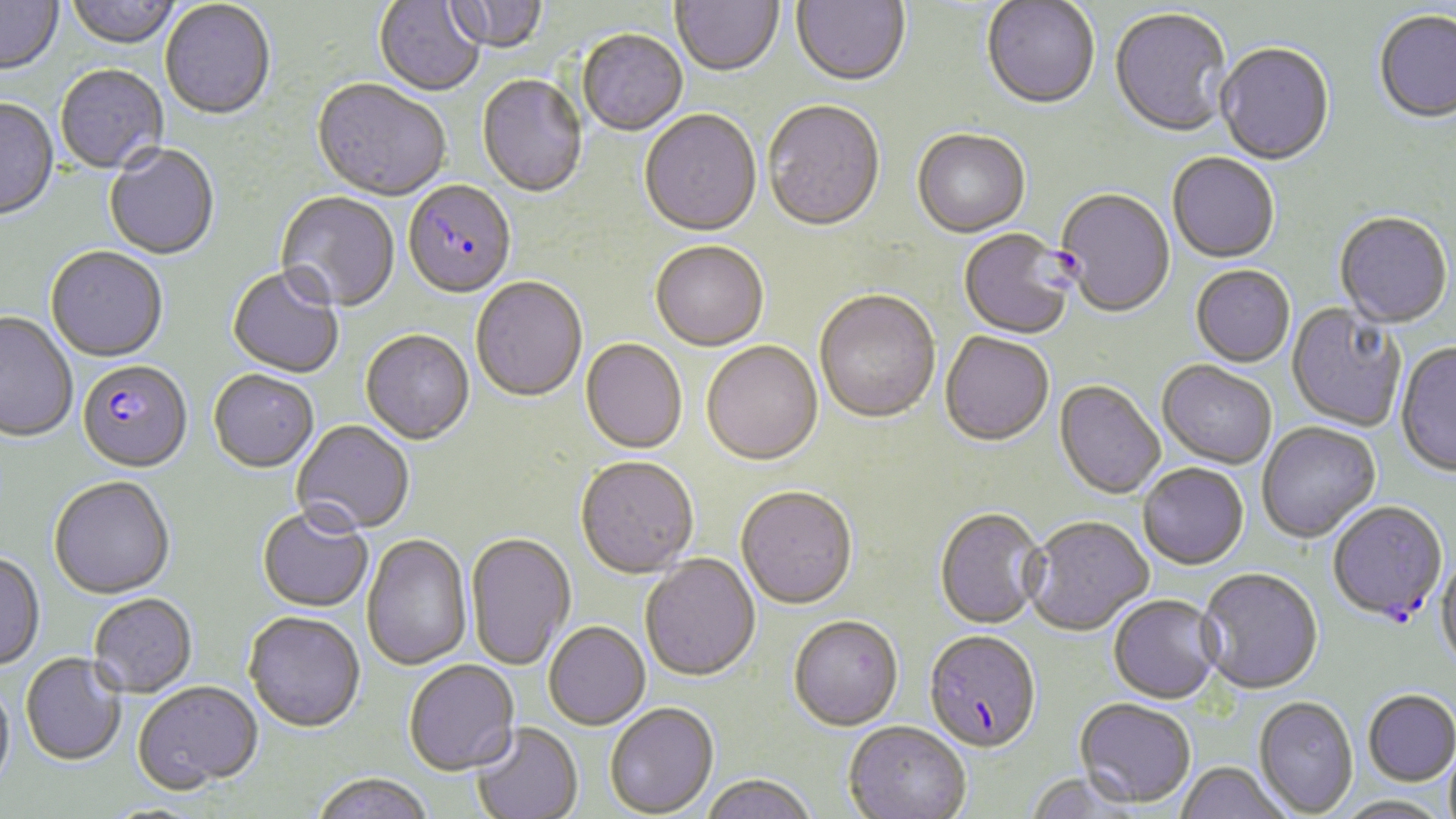
Approximate bounding boxes as (x1, y1, x2, y2) in pixels. Plasmodium falciparum-infected red blood cell locations: (403, 183, 516, 300), (958, 230, 1075, 342), (77, 362, 192, 475), (1328, 503, 1448, 626), (923, 634, 1042, 757). Uninfected red blood cell locations: (0, 0, 63, 77), (65, 0, 182, 51), (374, 0, 485, 98), (442, 0, 548, 55), (671, 0, 784, 79), (791, 0, 910, 89), (981, 1, 1100, 112), (160, 2, 275, 123), (1109, 9, 1232, 140), (1374, 12, 1456, 126), (578, 31, 688, 137), (1216, 45, 1335, 167), (56, 66, 168, 175), (477, 75, 588, 200), (312, 81, 451, 204), (0, 100, 60, 223), (763, 102, 886, 235), (639, 111, 762, 239), (912, 130, 1030, 239), (104, 145, 220, 261), (1167, 154, 1280, 265), (1055, 189, 1175, 320), (275, 192, 400, 315), (1334, 214, 1452, 329), (650, 243, 769, 353), (45, 249, 168, 365), (1191, 266, 1296, 369), (226, 269, 344, 380), (471, 278, 588, 404), (814, 292, 941, 426), (1287, 302, 1407, 432), (0, 313, 78, 444), (361, 331, 474, 446), (939, 333, 1054, 449), (580, 340, 687, 455), (701, 342, 823, 468), (1395, 343, 1456, 478), (1157, 363, 1276, 470), (208, 372, 318, 474), (1054, 382, 1165, 500), (292, 421, 415, 537), (1258, 423, 1381, 544), (575, 459, 699, 581), (1138, 465, 1249, 572), (49, 479, 175, 601), (736, 489, 858, 612), (257, 508, 373, 615), (934, 509, 1046, 631), (1023, 518, 1155, 638), (465, 533, 576, 672), (362, 535, 473, 671), (0, 553, 45, 673), (640, 554, 761, 684), (1436, 558, 1456, 673), (1197, 570, 1323, 697), (88, 595, 198, 699), (1108, 597, 1224, 706), (243, 614, 365, 735), (788, 618, 904, 733), (544, 623, 651, 731), (20, 654, 127, 767), (404, 661, 519, 777), (0, 681, 15, 794), (133, 683, 263, 795), (1363, 693, 1456, 788), (1253, 699, 1358, 817), (1073, 700, 1196, 809), (605, 704, 718, 817), (471, 723, 583, 819), (843, 724, 971, 819), (1176, 764, 1290, 819), (1024, 773, 1140, 819), (309, 774, 435, 819), (701, 776, 817, 819), (1334, 797, 1452, 819). Slide-level diagnosis: Plasmodium falciparum. Thin blood film. Image is 1456×819 pixels. Optical microscopy. Single field of view. Captured at 1000x magnification. May-Grünwald-Giemsa-stained preparation.